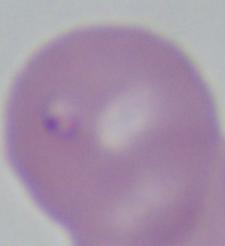
modality = micrograph
identification = Babesia
magnification = 1000x